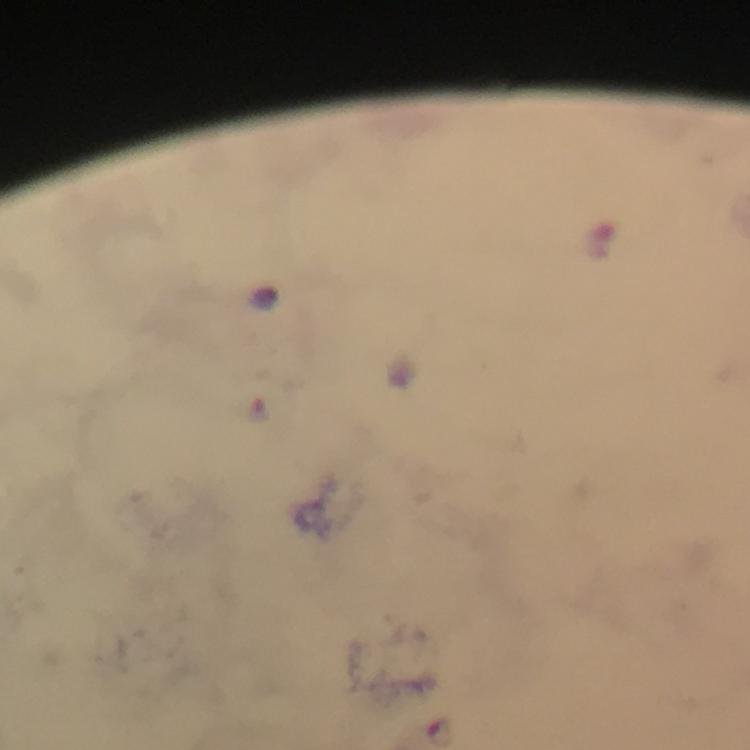
Approximate object centers, in pixels from the top-left corner.
Summary:
  - Malaria parasite locations: (x=441, y=731)
  - Magnification: 100x
  - Preparation: thick smear
  - Capture: smartphone mounted on the microscope
  - Image size: 750×750 pixels
  - Stain: Giemsa
  - Cropped from: one field of view
  - Immersion oil: applied
  - Context: from a diagnostic examination for malaria